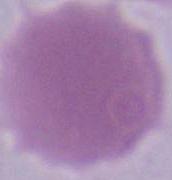

identification = red blood cell
magnification = 1000x
modality = micrograph